Give the position of every Plasmodium parasite visible.
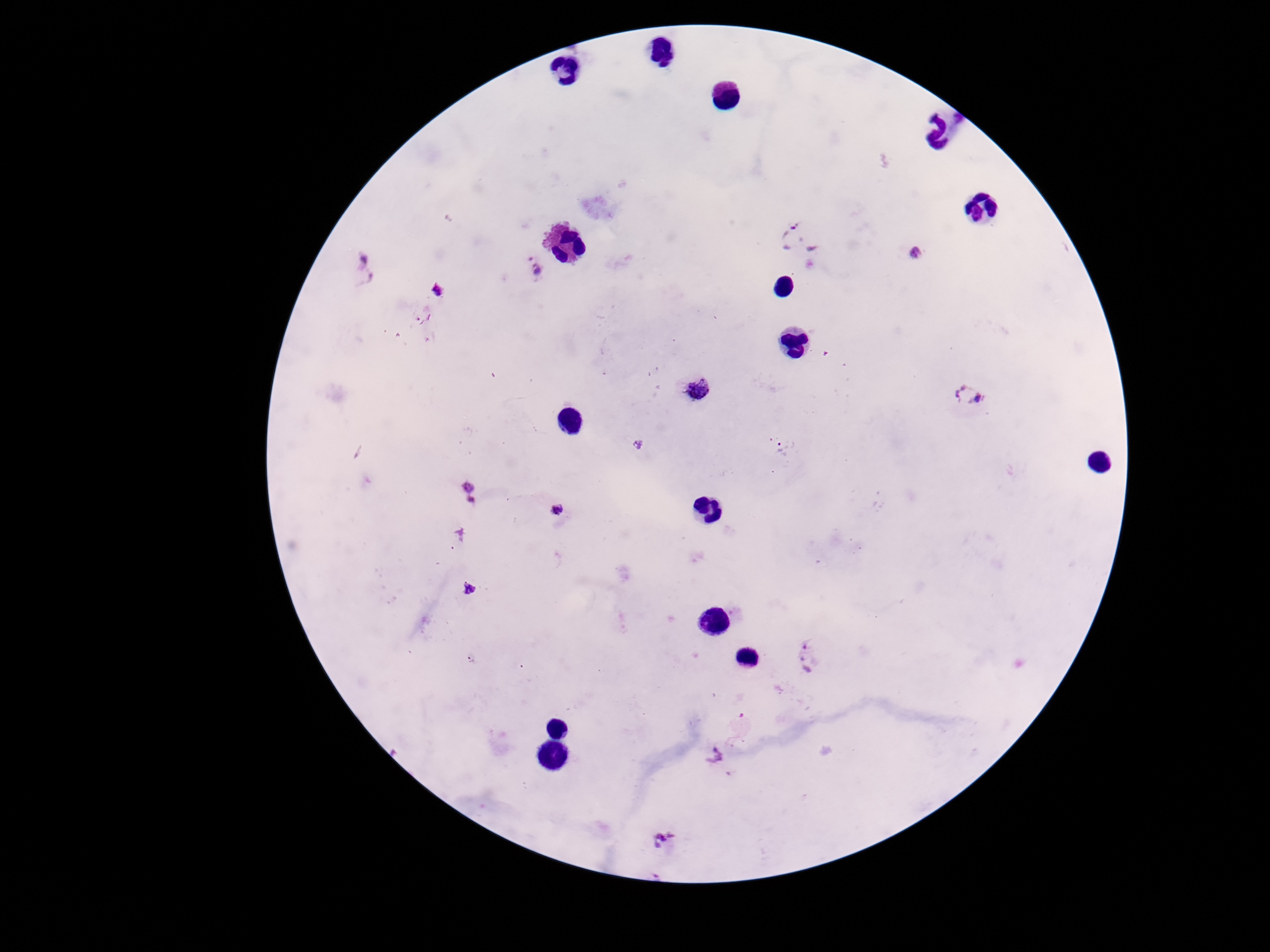

Approximate centers as [x, y] in pixels.
Plasmodium parasites: [800, 235], [917, 252], [534, 266], [364, 268], [440, 292], [694, 388], [968, 395], [638, 445], [785, 448], [466, 493], [556, 511], [470, 589], [810, 657], [714, 755], [666, 842].

Summary:
  - Capture: smartphone camera through the microscope eyepiece
  - Stain: Giemsa
  - Preparation: thick blood smear
  - Field of view: single
  - Magnification: 100x
  - Image size: 1270×952 pixels
  - Patient malaria status: infected